Locate and identify every blood parasite.
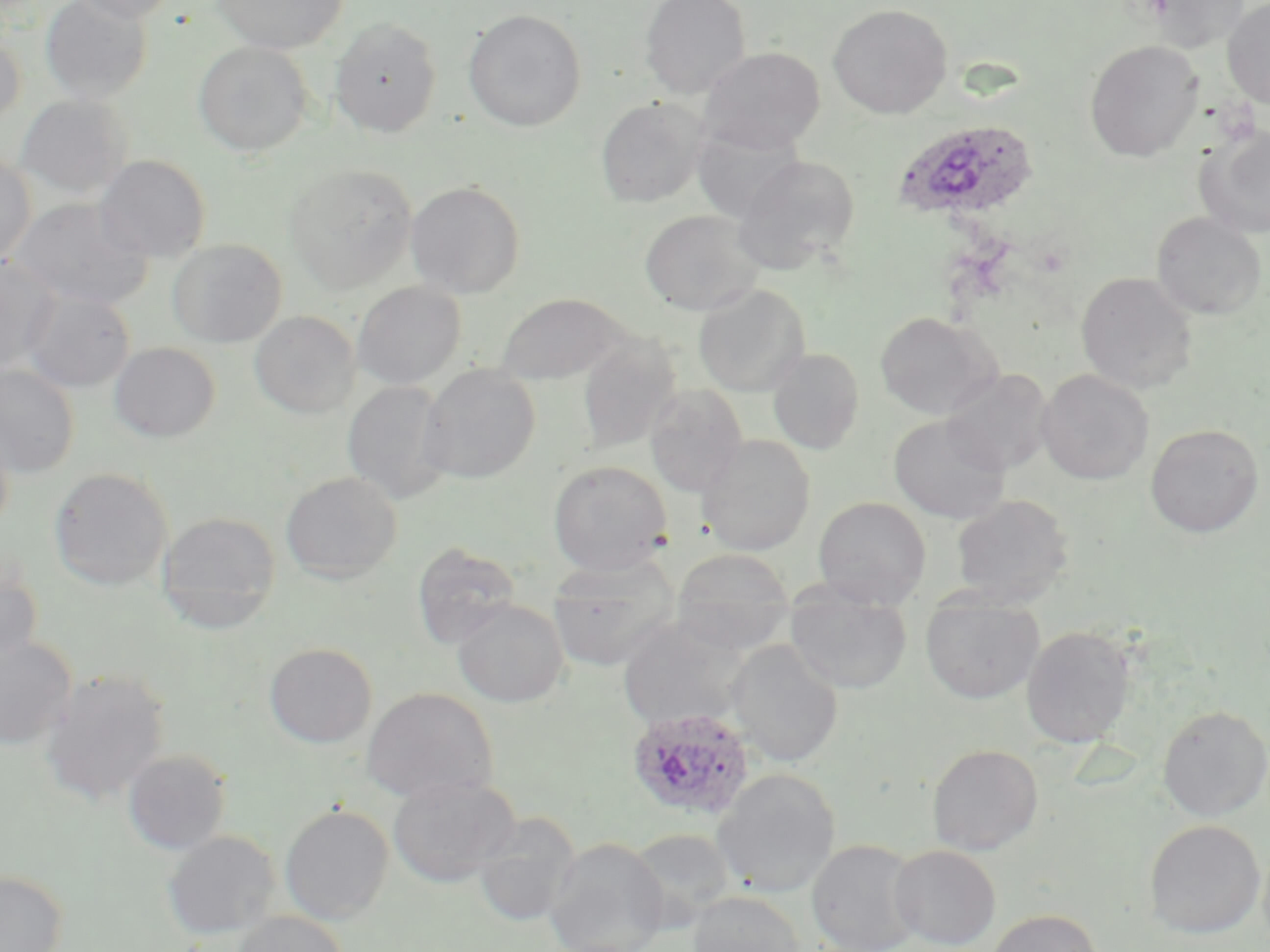
Approximate bounding boxes as [x1, y1, x2, y2] in pixels.
Plasmodium ovale-infected red blood cells: [894, 119, 1040, 222], [625, 706, 758, 822].
No Plasmodium falciparum, Plasmodium malariae, Plasmodium vivax, Babesia divergens, or Trypanosoma brucei observed.

Uninfected red blood cell locations: [40, 0, 152, 104], [70, 0, 182, 24], [212, 0, 348, 54], [640, 0, 751, 99], [1222, 0, 1270, 109], [1145, 1, 1248, 53], [827, 3, 953, 119], [463, 9, 586, 131], [330, 16, 442, 138], [0, 31, 26, 128], [1084, 39, 1203, 162], [193, 41, 313, 156], [698, 46, 826, 153], [15, 94, 133, 199], [595, 97, 709, 207], [1194, 122, 1270, 239], [0, 150, 36, 266], [95, 154, 212, 263], [731, 154, 862, 274], [285, 163, 418, 293], [406, 180, 526, 298], [11, 198, 152, 310], [640, 209, 763, 316], [1151, 212, 1266, 319], [167, 239, 287, 348], [0, 255, 62, 373], [1076, 271, 1197, 393], [352, 282, 467, 389], [693, 284, 810, 396], [23, 291, 135, 393], [494, 292, 632, 385], [250, 311, 360, 418], [875, 311, 1001, 420], [577, 335, 681, 454], [109, 342, 221, 442], [767, 348, 865, 454], [419, 363, 541, 483], [0, 364, 81, 477], [942, 368, 1054, 475], [1036, 369, 1154, 485], [342, 381, 453, 504], [643, 384, 748, 497], [0, 412, 16, 533], [889, 415, 1011, 524], [1145, 423, 1265, 537], [698, 434, 816, 555], [548, 459, 673, 576], [48, 467, 173, 591], [281, 470, 402, 583], [950, 493, 1074, 608], [812, 496, 931, 608], [156, 511, 281, 631], [411, 542, 522, 649], [671, 548, 795, 655], [546, 556, 681, 671], [0, 558, 43, 667], [785, 583, 912, 695], [920, 594, 1044, 704], [452, 599, 569, 708], [617, 618, 749, 732], [1020, 625, 1136, 748], [0, 634, 77, 751], [727, 638, 843, 767], [264, 642, 377, 748], [38, 668, 171, 808], [361, 687, 498, 803], [1157, 705, 1270, 820], [927, 743, 1043, 855], [122, 749, 232, 855], [712, 768, 841, 897], [387, 775, 521, 887], [280, 804, 395, 924], [472, 812, 581, 927], [1144, 820, 1266, 938], [627, 828, 736, 929], [162, 830, 281, 940], [544, 837, 670, 952], [806, 839, 924, 952], [889, 844, 1001, 950], [0, 870, 67, 952], [689, 890, 805, 952], [987, 908, 1101, 952], [230, 911, 349, 952]. Slide-level diagnosis: Plasmodium ovale. Image is 1270×952 pixels. Single field of view. May-Grünwald-Giemsa-stained preparation. 1000x magnification. Thin blood film. Light microscopy.